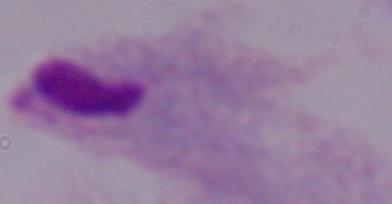
magnification = 1000x
modality = micrograph
identification = trichomonad